Outline each blood parasite and name the species.
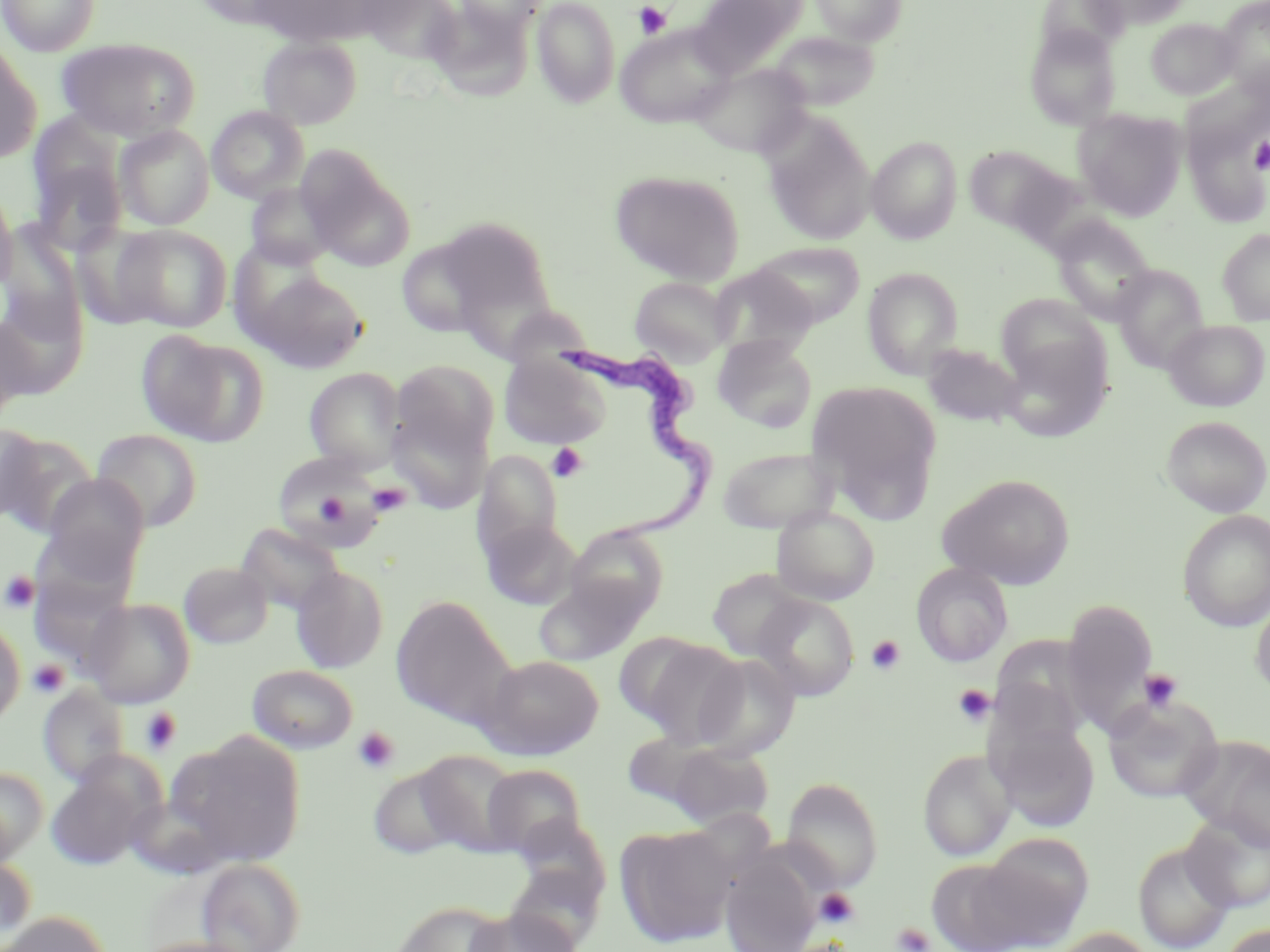
Approximate bounding boxes as (x1, y1, x2, y2) in pixels.
Trypanosoma brucei: (558, 341, 718, 554).
No Plasmodium falciparum, Plasmodium ovale, Plasmodium malariae, Plasmodium vivax, or Babesia divergens observed.

Summary:
  - Platelet locations: (633, 1, 671, 39), (1250, 137, 1270, 174), (547, 443, 588, 483), (368, 481, 411, 517), (317, 496, 352, 527), (1, 571, 40, 613), (866, 635, 905, 675), (27, 659, 70, 699), (1138, 668, 1183, 713), (952, 684, 996, 727), (139, 706, 181, 754), (352, 726, 400, 773), (814, 888, 859, 929), (892, 922, 935, 952)
  - Uninfected red blood cell locations: (0, 0, 101, 56), (247, 0, 393, 49), (358, 0, 465, 65), (454, 0, 545, 37), (532, 0, 620, 108), (690, 0, 808, 76), (810, 0, 907, 45), (1084, 0, 1192, 29), (1215, 0, 1270, 91), (1145, 17, 1239, 99), (615, 25, 735, 128), (1025, 26, 1122, 130), (769, 31, 880, 111), (258, 37, 361, 129), (56, 38, 198, 141), (0, 41, 41, 164), (691, 62, 810, 159), (206, 105, 308, 203), (1073, 109, 1186, 219), (762, 115, 876, 245), (114, 124, 214, 230), (26, 126, 129, 258), (867, 136, 962, 243), (964, 146, 1063, 231), (299, 150, 414, 271), (610, 169, 745, 285), (0, 183, 19, 296), (245, 183, 340, 270), (436, 216, 553, 318), (1051, 217, 1156, 323), (113, 224, 232, 332), (1217, 228, 1270, 325), (395, 237, 499, 340), (752, 241, 866, 328), (1111, 264, 1209, 370), (708, 265, 819, 357), (862, 267, 964, 378), (254, 272, 369, 373), (629, 276, 734, 365), (994, 293, 1106, 389), (499, 304, 593, 368), (0, 314, 36, 421), (1164, 319, 1269, 411), (137, 332, 269, 447), (998, 335, 1112, 442), (713, 337, 817, 433), (921, 343, 1025, 428), (499, 355, 611, 449), (392, 360, 499, 459), (304, 367, 406, 473), (807, 379, 942, 518), (385, 408, 492, 513), (1161, 415, 1270, 517), (0, 423, 47, 526), (90, 429, 202, 531), (0, 432, 97, 535), (716, 444, 840, 533), (472, 449, 563, 562), (271, 451, 389, 551), (937, 473, 1076, 589), (41, 474, 149, 577), (771, 506, 879, 605), (1178, 510, 1270, 632), (479, 516, 581, 610), (236, 522, 346, 618), (565, 525, 669, 623), (179, 561, 273, 648), (911, 562, 1014, 668), (291, 566, 389, 672), (706, 568, 811, 661), (533, 575, 648, 667), (752, 594, 860, 702), (390, 596, 513, 726), (82, 597, 196, 708), (1251, 597, 1270, 699), (1061, 600, 1158, 734), (0, 617, 25, 729), (614, 632, 709, 725), (989, 633, 1097, 738), (636, 639, 747, 748), (693, 653, 800, 760), (482, 654, 604, 760), (247, 664, 358, 753), (38, 685, 130, 787), (1102, 694, 1223, 805), (989, 717, 1101, 832), (620, 731, 723, 815), (170, 733, 307, 867), (1178, 734, 1270, 849), (663, 743, 775, 829), (413, 749, 522, 855), (918, 749, 1016, 861), (45, 764, 156, 869), (367, 764, 469, 860), (481, 764, 587, 859), (0, 766, 49, 864), (782, 777, 883, 892), (1181, 813, 1270, 913), (615, 824, 737, 947), (975, 834, 1093, 946), (1133, 841, 1235, 952), (0, 853, 37, 948), (721, 857, 818, 952), (196, 858, 306, 952), (927, 859, 1036, 952), (502, 864, 604, 950), (390, 900, 511, 952), (463, 907, 581, 952), (0, 912, 112, 952), (1219, 923, 1270, 952), (1050, 927, 1155, 952), (133, 936, 262, 952)
  - Slide-level diagnosis: Trypanosoma brucei
  - Modality: optical microscopy
  - Field of view: one of a larger specimen
  - Image size: 1270×952 pixels
  - Magnification: 1000x
  - Preparation: thin blood smear
  - Stain: May-Grünwald-Giemsa